Report the malaria status of this cell.
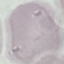
It is uninfected.

Automatically extracted cell patch, resized to 64 × 64 pixels. Photographed with a smartphone camera at the microscope eyepiece. Thin smear of blood. Giemsa stain.